Assess this cell for malaria.
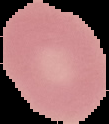

It is uninfected.

preparation = thin blood film
image type = segmented cell region with the area outside set to black
image size = 109×124 pixels